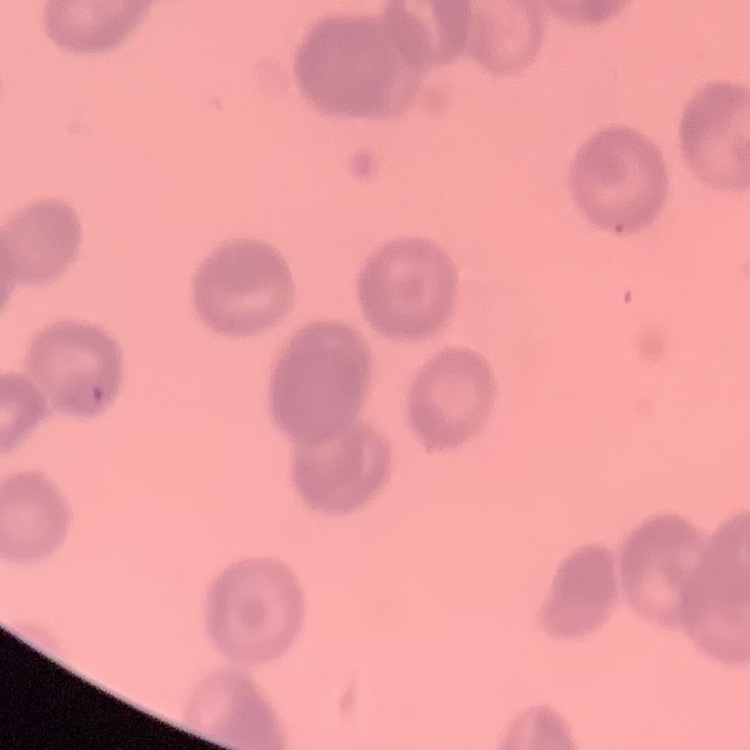

red blood cell morphology = rouleaux formation
preparation = thin blood film
image type = one tile cut from a larger photomicrograph
stain = Field's or Giemsa